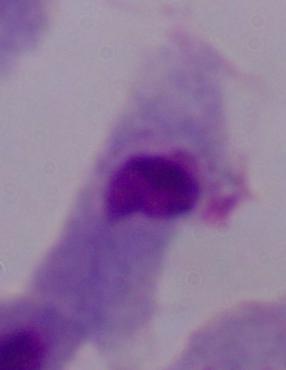

Summary:
  - Modality: micrograph
  - Identification: trichomonad
  - Magnification: 1000x